Report the malaria status.
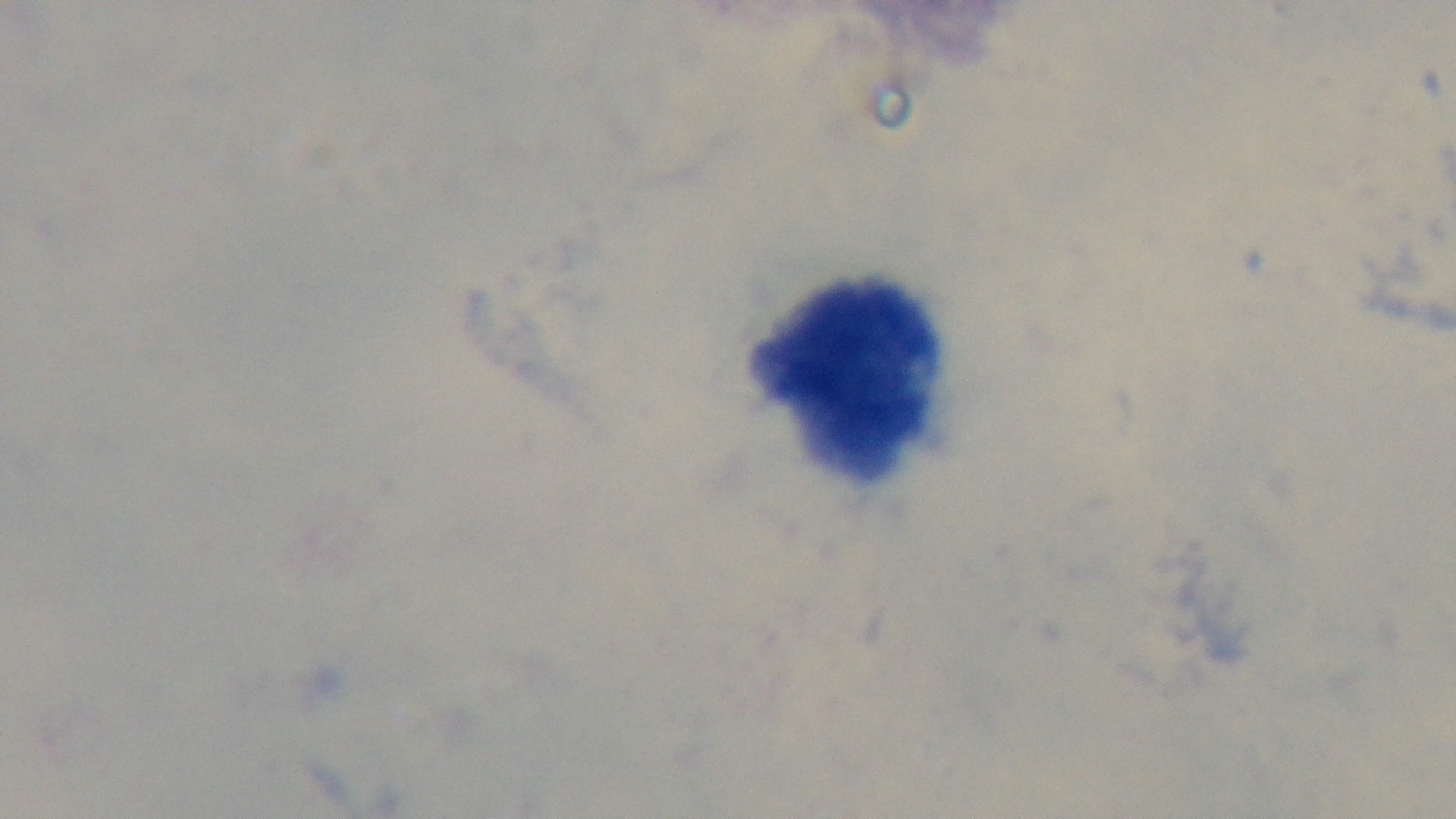

It is uninfected.

stain = Giemsa
objective = 100x oil immersion
capture = mounted 4K digital camera
field of view = one from the slide
preparation = thick smear
modality = light microscopy